Comment on the morphology of the erythrocytes.
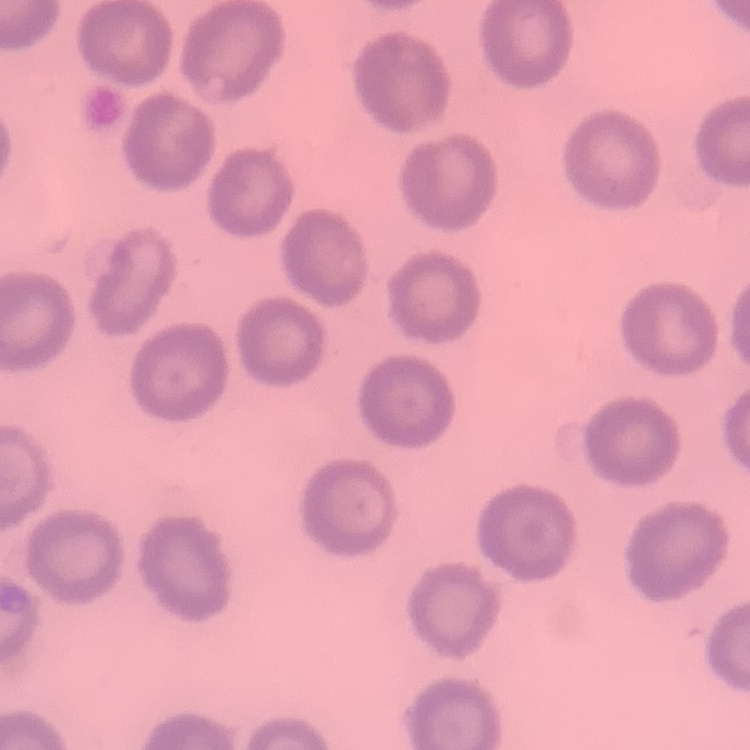

They show no rouleaux formation.

Square crop of a larger photomicrograph. Thin blood film. Field's or Giemsa stain.